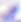
Summary:
  - Modality: photomicrograph
  - Magnification: 400x
  - Identification: Toxoplasma gondii